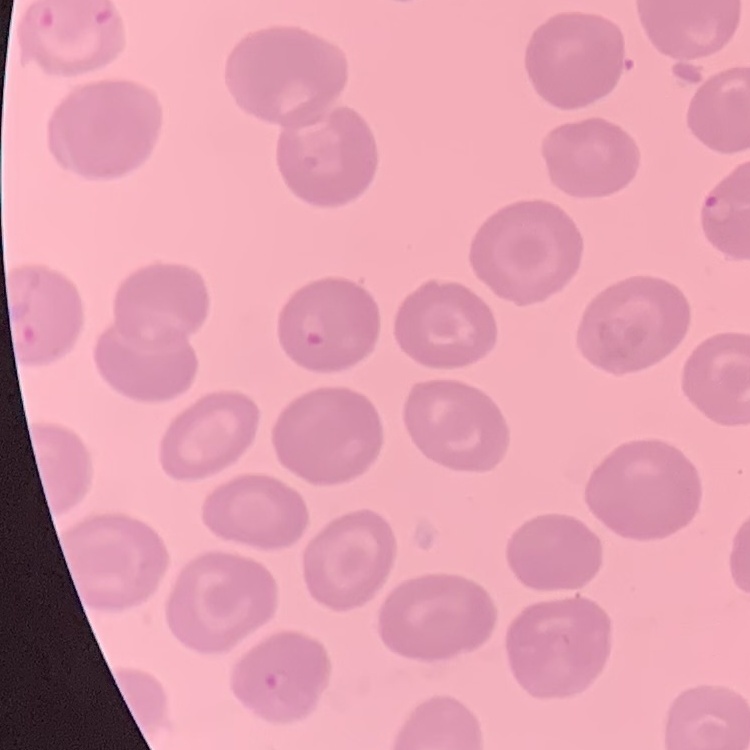
Summary:
  - Erythrocyte morphology: no rouleaux formation
  - Image type: one tile cut from a larger photomicrograph
  - Stain: Field's or Giemsa
  - Preparation: thin peripheral smear